Assess this cell for malaria.
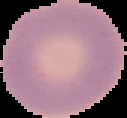

Uninfected.

Summary:
  - Preparation: thin blood smear
  - Image size: 127×118 pixels
  - Image type: cell region segmented out of the field of view; surrounding area masked to black